State which parasite is depicted.
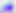
Toxoplasma gondii.

Summary:
  - Modality: photomicrograph
  - Magnification: 400x